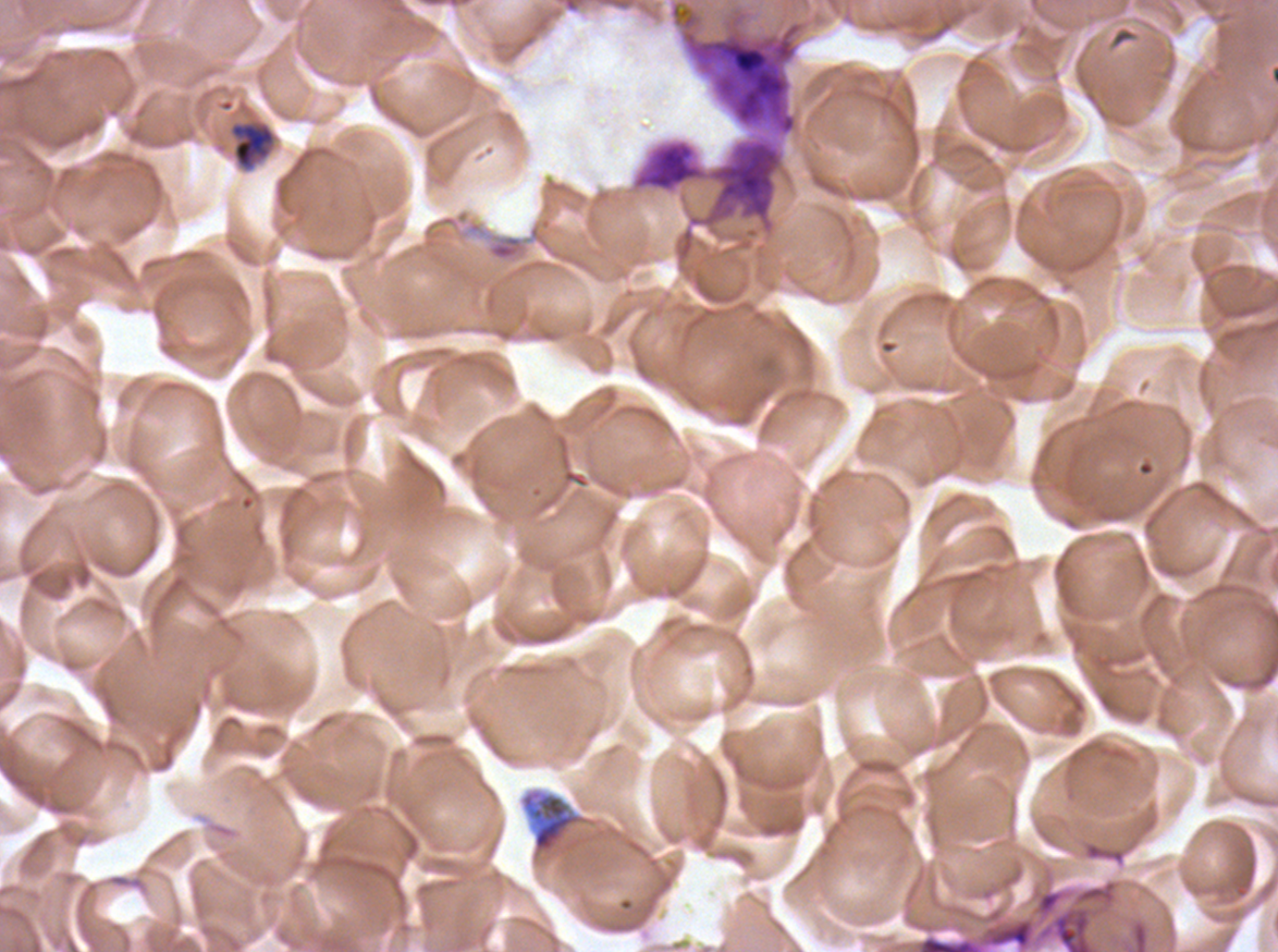 Approximate bounding rectangles given as corner coordinates in pixels from the top-left. Debris locations: (x1=521, y1=788, x2=584, y2=855). Mid trophozoite locations: (x1=229, y1=122, x2=276, y2=170). Thin blood smear. Image is 1278×952 pixels. Giemsa-stained preparation. One sub-image of a larger composite. Plasmodium falciparum from a patient in The Gambia, cultured ex vivo for 24 to 48 hours.